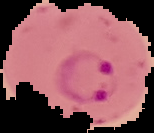

image type = segmented cell region on a black background
preparation = thin blood smear
result = Plasmodium parasites detected
image size = 154×133 pixels